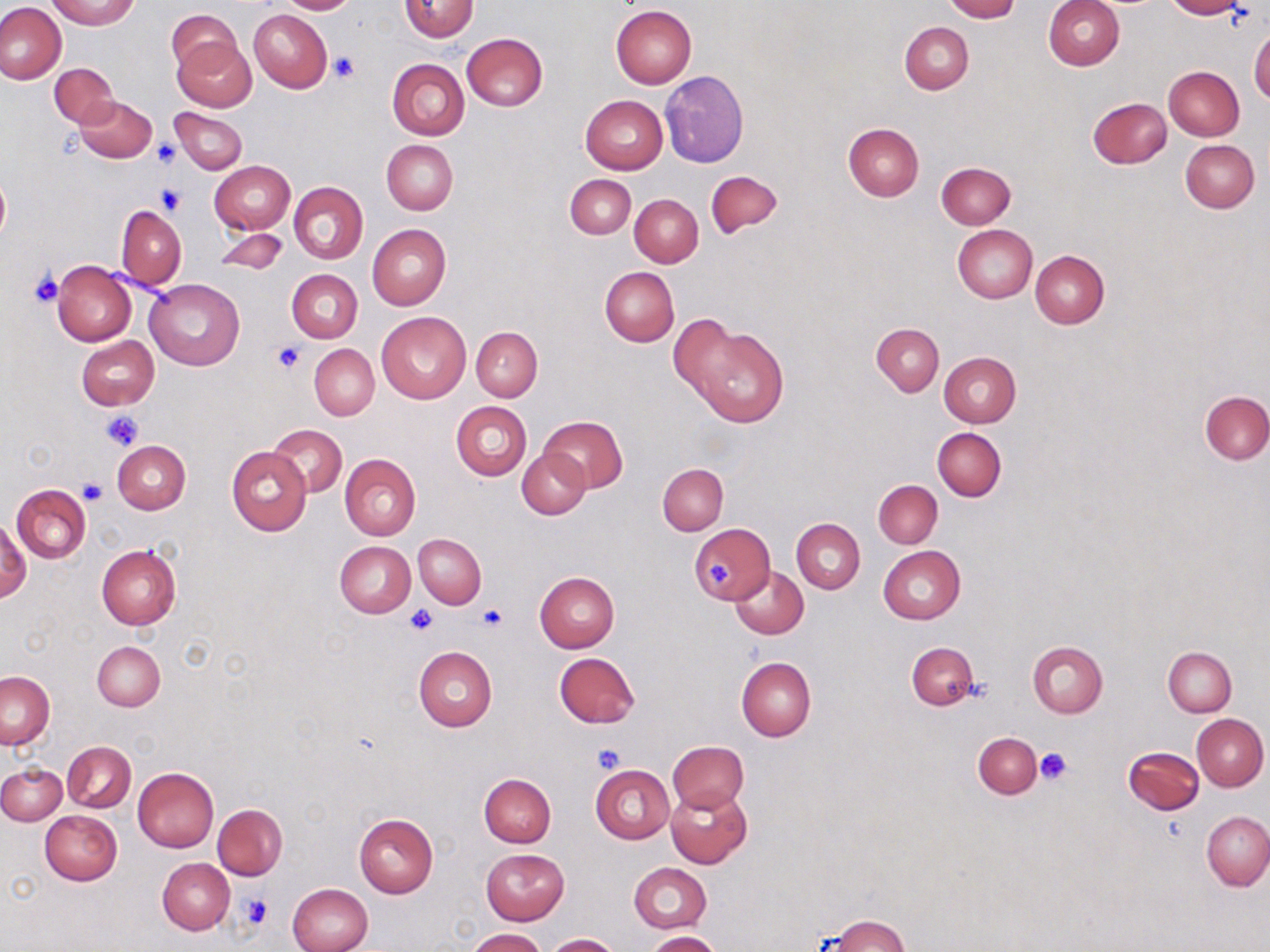 Approximate bounding boxes as [x1, y1, x2, y2] in pixels. Platelet locations: [330, 51, 361, 83], [152, 140, 180, 168], [155, 186, 187, 216], [29, 268, 63, 309], [272, 342, 304, 373], [100, 410, 145, 451], [78, 478, 106, 504], [706, 560, 731, 587], [477, 604, 506, 631], [408, 607, 436, 634], [591, 744, 623, 773], [1035, 747, 1072, 785], [239, 892, 272, 929]. Uninfected red blood cell locations: [48, 0, 139, 28], [274, 0, 359, 14], [400, 0, 478, 42], [942, 0, 1021, 22], [1043, 0, 1124, 69], [1165, 0, 1243, 19], [1, 3, 67, 85], [611, 4, 697, 88], [168, 9, 238, 75], [249, 9, 332, 92], [901, 22, 973, 94], [1249, 28, 1270, 106], [462, 33, 547, 112], [171, 35, 256, 112], [387, 58, 468, 141], [50, 63, 119, 128], [1164, 66, 1244, 141], [660, 70, 749, 167], [73, 94, 157, 163], [580, 94, 668, 174], [1088, 97, 1172, 168], [171, 107, 247, 175], [843, 123, 924, 202], [1180, 139, 1259, 213], [382, 140, 458, 215], [209, 160, 294, 234], [936, 162, 1016, 229], [0, 171, 10, 246], [707, 171, 782, 237], [565, 174, 635, 239], [289, 182, 368, 264], [630, 194, 702, 267], [116, 205, 186, 289], [367, 223, 451, 310], [953, 225, 1037, 303], [214, 226, 289, 277], [1030, 250, 1109, 329], [52, 261, 136, 345], [599, 266, 678, 346], [286, 269, 361, 343], [145, 277, 245, 370], [376, 310, 471, 403], [676, 321, 789, 427], [871, 323, 945, 396], [471, 326, 541, 401], [75, 335, 159, 410], [309, 344, 379, 420], [939, 352, 1021, 428], [1201, 390, 1270, 464], [451, 401, 532, 480], [540, 416, 627, 493], [267, 423, 347, 498], [933, 428, 1006, 501], [113, 440, 191, 514], [226, 446, 312, 534], [518, 449, 589, 519], [339, 454, 420, 541], [657, 463, 728, 535], [873, 480, 943, 548], [12, 484, 91, 563], [1, 517, 30, 603], [793, 519, 865, 594], [690, 524, 774, 604], [414, 533, 486, 609], [335, 541, 416, 617], [97, 545, 181, 630], [878, 545, 965, 624], [730, 566, 808, 639], [534, 571, 620, 652], [1028, 641, 1108, 717], [92, 642, 165, 710], [906, 643, 979, 711], [414, 645, 497, 731], [1164, 646, 1236, 716], [553, 652, 641, 728], [737, 657, 816, 741], [1, 672, 54, 749], [1193, 713, 1269, 791], [972, 732, 1041, 799], [667, 740, 748, 814], [63, 741, 135, 813], [1124, 746, 1203, 815], [0, 763, 65, 824], [590, 765, 674, 845], [133, 767, 219, 851], [480, 774, 556, 847], [666, 787, 751, 869], [212, 804, 287, 880], [1201, 810, 1269, 891], [41, 811, 122, 884], [354, 813, 439, 898], [481, 849, 569, 925], [157, 857, 234, 935], [629, 862, 712, 934], [286, 884, 372, 952], [826, 915, 910, 952], [468, 928, 546, 952], [647, 932, 721, 951], [546, 933, 619, 951]. Slide-level diagnosis: no evidence of blood parasites. May-Grünwald-Giemsa stain. Optical microscopy. One field of a larger specimen. Image is 1270×952 pixels. 1000x magnification. Thin blood smear.